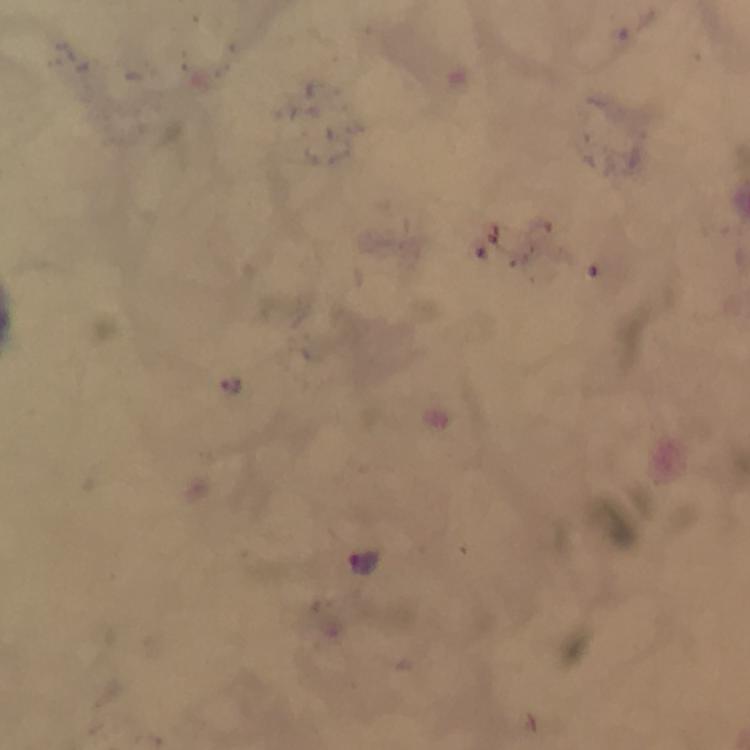
immersion oil = used
image size = 750×750 pixels
Plasmodium parasite locations = approximate centers as (x, y) in pixels: (230, 387), (364, 565)
capture = smartphone camera through the microscope
magnification = 100x
cropped from = one field of view
context = from a malaria diagnostic workup
preparation = thick blood smear
stain = Giemsa